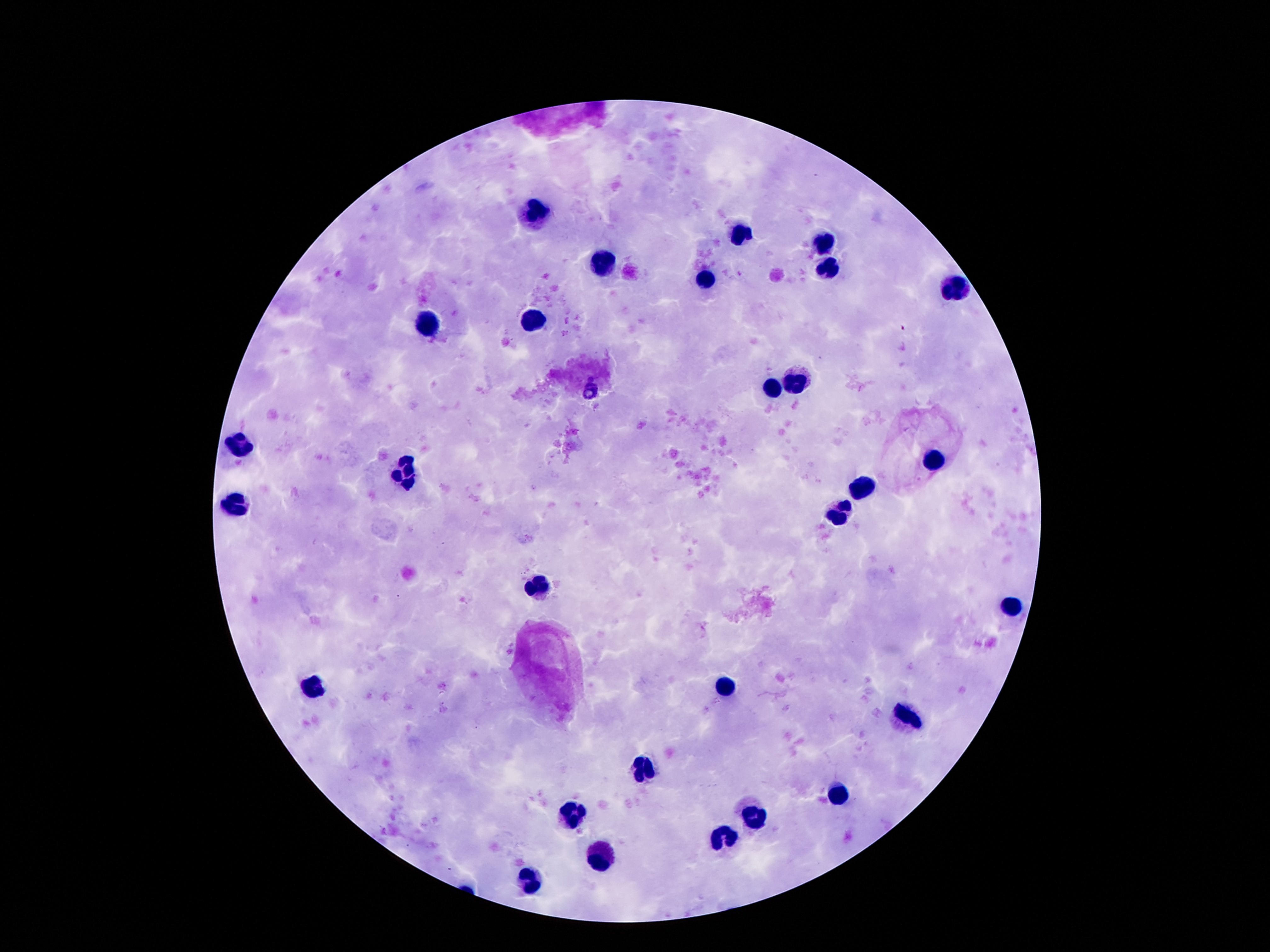

Approximate centers as {x, y} in pixels. Leukocyte locations: {537, 210}, {742, 232}, {824, 246}, {605, 265}, {828, 269}, {707, 279}, {955, 287}, {537, 320}, {422, 324}, {793, 379}, {771, 388}, {242, 442}, {932, 459}, {410, 470}, {859, 490}, {236, 502}, {840, 512}, {537, 587}, {1010, 607}, {723, 685}, {309, 686}, {906, 717}, {643, 768}, {838, 794}, {574, 813}, {756, 815}, {723, 838}, {598, 856}, {529, 881}. Photographed through the microscope eyepiece with a smartphone camera. Patient malaria status: not infected. 100x magnification. Giemsa-stained preparation. One field from this slide. Image is 1270×952 pixels. Thick peripheral-blood smear.